Describe the morphology of the erythrocytes.
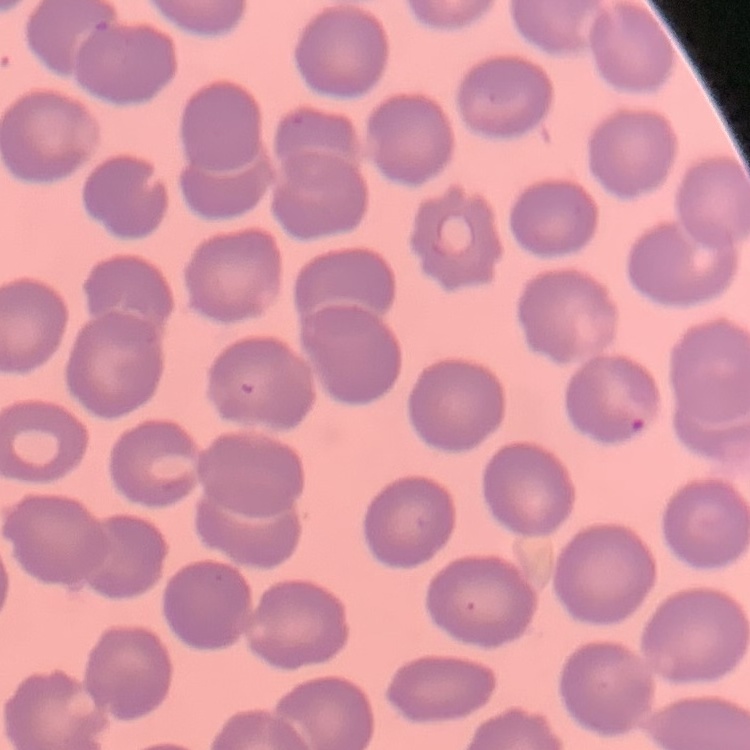

They show no rouleaux formation.

Field's or Giemsa stain. Thin blood film. One tile cut from a larger photomicrograph.